Identify the blood parasite species.
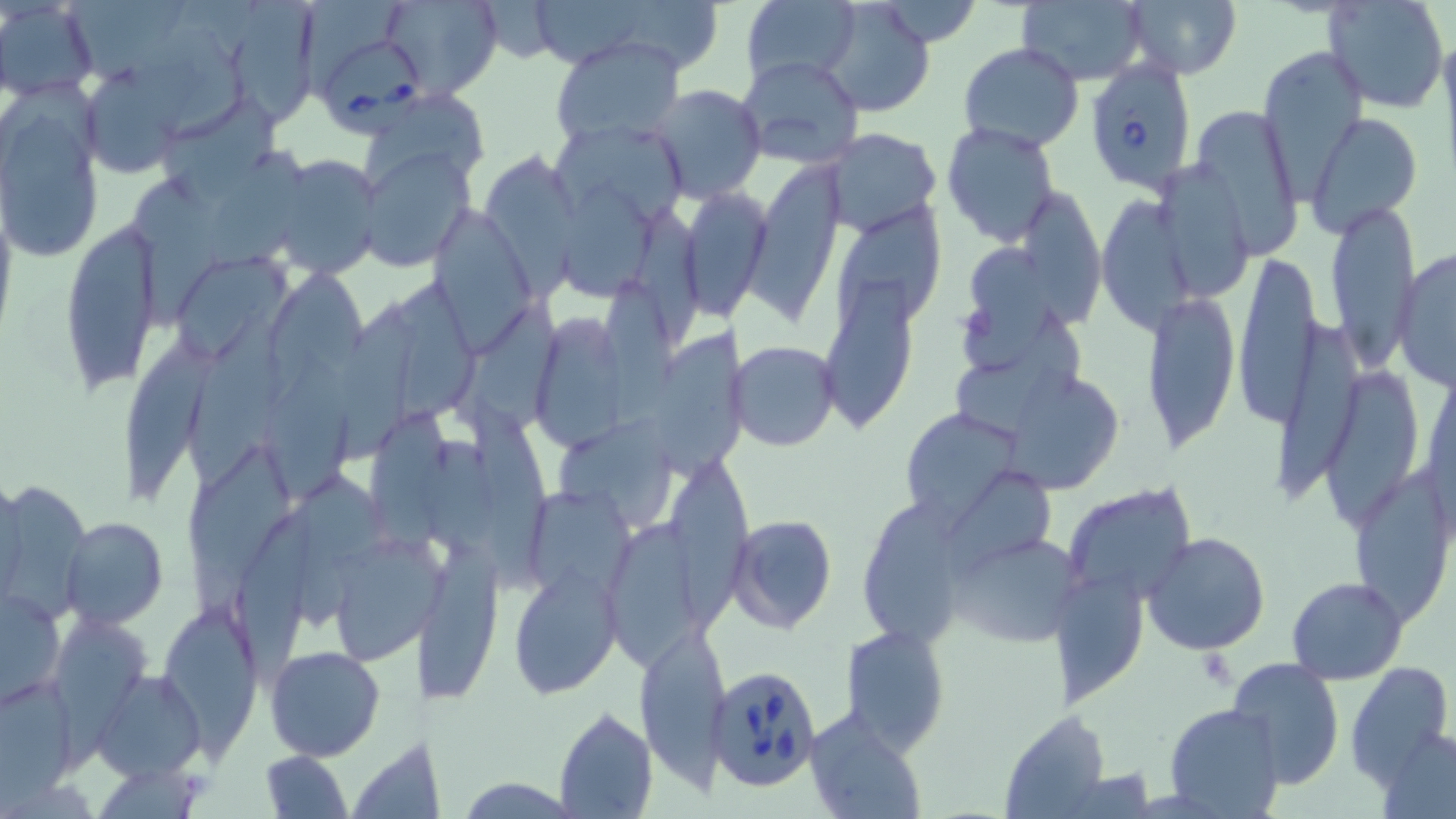

Babesia divergens.

Approximate bounding boxes as (x1, y1, x2, y2) in pixels. Uninfected red blood cell locations: (0, 0, 99, 100), (64, 0, 188, 88), (384, 0, 501, 97), (476, 0, 562, 63), (1015, 0, 1148, 86), (1122, 0, 1241, 79), (1324, 0, 1450, 113), (740, 1, 858, 88), (820, 1, 936, 117), (864, 2, 988, 45), (233, 3, 323, 125), (145, 15, 245, 143), (551, 36, 686, 144), (957, 42, 1085, 153), (1259, 44, 1366, 186), (736, 54, 866, 172), (81, 69, 184, 180), (649, 85, 767, 203), (358, 89, 491, 200), (2, 92, 105, 264), (162, 95, 278, 209), (1190, 103, 1304, 259), (1307, 112, 1422, 238), (556, 118, 687, 227), (942, 122, 1062, 247), (823, 127, 941, 234), (360, 146, 474, 269), (202, 148, 314, 278), (266, 154, 383, 279), (483, 158, 587, 307), (745, 163, 843, 323), (1152, 163, 1253, 300), (130, 173, 219, 328), (562, 181, 658, 306), (674, 185, 774, 320), (1027, 188, 1104, 332), (1096, 194, 1198, 338), (638, 202, 705, 342), (1323, 203, 1419, 377), (837, 207, 942, 336), (431, 208, 533, 344), (60, 221, 162, 394), (959, 245, 1052, 376), (1393, 247, 1455, 389), (180, 252, 285, 360), (1230, 252, 1326, 437), (275, 269, 373, 389), (820, 276, 915, 428), (598, 277, 682, 436), (397, 287, 478, 431), (1142, 290, 1241, 454), (459, 300, 562, 437), (332, 304, 424, 469), (187, 311, 288, 498), (950, 312, 1083, 447), (540, 313, 624, 447), (1276, 317, 1361, 499), (650, 327, 750, 483), (123, 338, 216, 509), (730, 340, 839, 451), (1324, 357, 1424, 528), (261, 360, 354, 501), (995, 372, 1132, 492), (464, 391, 552, 589), (372, 405, 450, 563), (898, 407, 1024, 522), (555, 410, 688, 530), (423, 426, 506, 565), (187, 439, 295, 622), (664, 456, 756, 647), (1348, 464, 1452, 622), (287, 465, 392, 636), (945, 465, 1062, 580), (5, 484, 95, 622), (1064, 486, 1196, 606), (529, 490, 638, 604), (865, 490, 969, 647), (727, 514, 838, 633), (604, 516, 721, 689), (61, 517, 167, 627), (945, 528, 1085, 651), (1142, 532, 1271, 656), (328, 536, 436, 666), (416, 541, 507, 703), (510, 565, 623, 699), (1054, 567, 1152, 705), (1286, 575, 1407, 685), (1, 585, 67, 709), (158, 604, 259, 745), (50, 614, 149, 734), (839, 621, 951, 753), (633, 623, 732, 781), (263, 647, 385, 762), (1226, 657, 1345, 789), (1342, 661, 1454, 792), (96, 669, 206, 780), (0, 675, 78, 792), (1164, 703, 1285, 816), (554, 708, 657, 819), (803, 708, 925, 819), (994, 709, 1106, 818), (1376, 723, 1456, 819), (347, 740, 429, 817), (259, 749, 353, 819), (458, 778, 579, 816). Platelet locations: (1190, 652, 1241, 687). Babesia divergens-infected red blood cell locations: (327, 43, 430, 138), (1085, 58, 1198, 191), (704, 664, 823, 793). One field of a larger specimen. May-Grünwald-Giemsa-stained preparation. Image is 1456×819 pixels. Thin blood film. Captured at 1000x magnification. Optical microscopy.